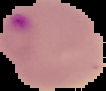
Result: Plasmodium parasites identified. From a thin blood smear. Image is 106×91 pixels. Segmented cell region on a black background.